State which cell type is depicted.
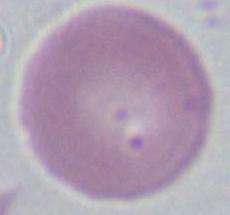

This is an erythrocyte.

Captured at 1000x magnification. Photomicrograph.